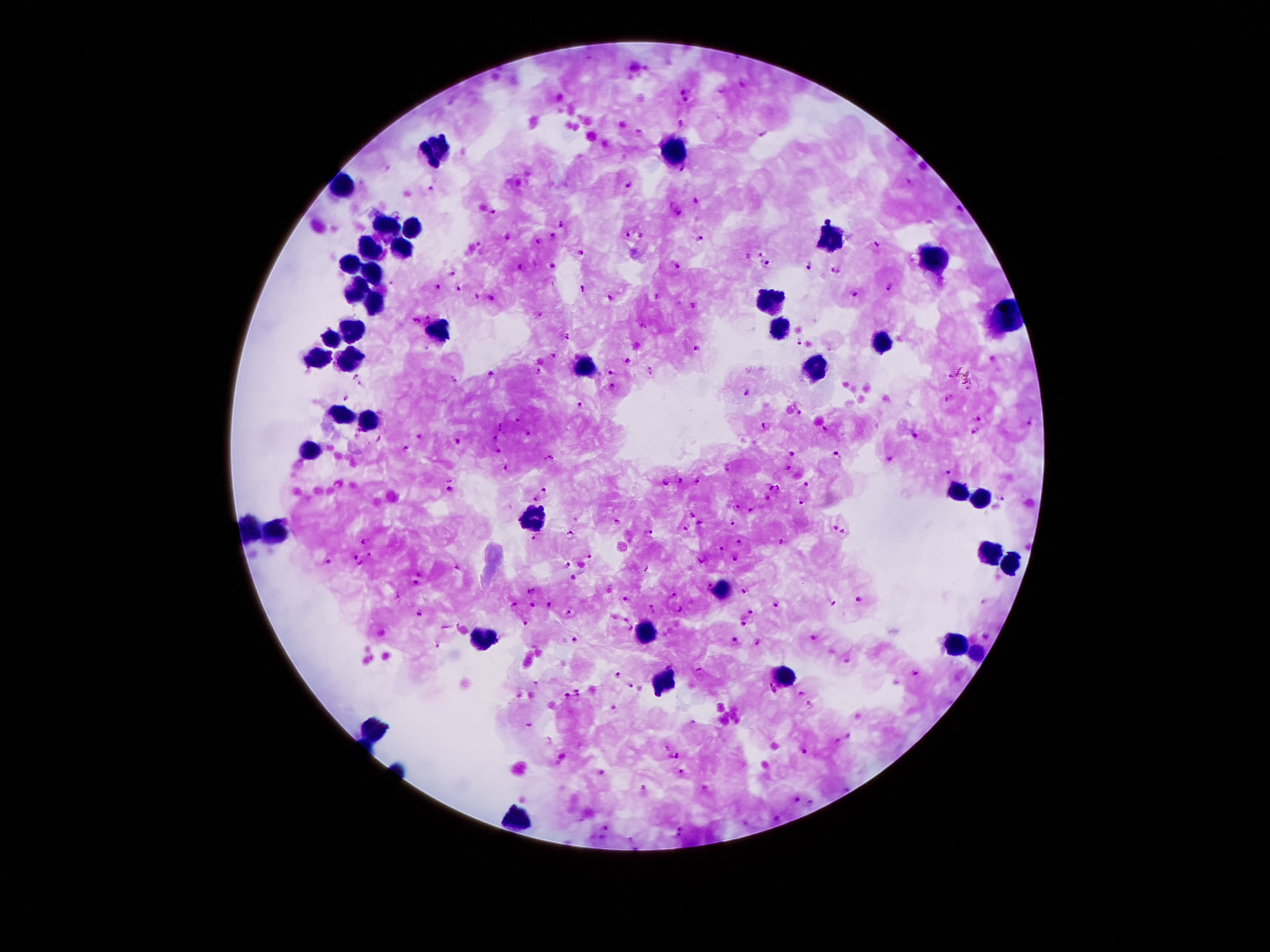
field_of_view: one from this slide
patient_malaria_status: infected with Plasmodium falciparum
malaria_parasite_locations: 'approximate object centers, in pixels from the top-left corner: (x=742, y=85), (x=681, y=93), (x=686, y=100), (x=683, y=124), (x=685, y=170), (x=630, y=184), (x=431, y=190), (x=698, y=202), (x=672, y=205), (x=959, y=211), (x=495, y=212), (x=681, y=214), (x=561, y=225), (x=628, y=235), (x=642, y=235), (x=552, y=236), (x=507, y=237), (x=701, y=239), (x=539, y=242), (x=877, y=244), (x=581, y=252), (x=761, y=255), (x=748, y=258), (x=553, y=265), (x=675, y=265), (x=768, y=265), (x=523, y=267), (x=809, y=267), (x=453, y=273), (x=834, y=273), (x=392, y=284), (x=439, y=288), (x=459, y=288), (x=890, y=288), (x=581, y=290), (x=856, y=294), (x=477, y=296), (x=492, y=297), (x=658, y=297), (x=612, y=299), (x=694, y=306), (x=537, y=315), (x=429, y=320), (x=414, y=322), (x=643, y=325), (x=567, y=335), (x=798, y=342), (x=696, y=350), (x=553, y=354), (x=628, y=361), (x=611, y=372), (x=650, y=372), (x=491, y=373), (x=538, y=373), (x=949, y=376), (x=357, y=378), (x=455, y=380), (x=362, y=386), (x=612, y=388), (x=748, y=394), (x=346, y=398), (x=949, y=400), (x=579, y=405), (x=800, y=414), (x=977, y=419), (x=517, y=421), (x=1030, y=423), (x=765, y=426), (x=501, y=427), (x=825, y=430), (x=975, y=432), (x=359, y=433), (x=528, y=435), (x=420, y=436), (x=914, y=436), (x=496, y=439), (x=458, y=441), (x=406, y=449), (x=499, y=451), (x=793, y=454), (x=836, y=454), (x=890, y=459), (x=552, y=461), (x=506, y=467), (x=788, y=468), (x=728, y=469), (x=946, y=470), (x=681, y=481), (x=698, y=481), (x=664, y=482), (x=808, y=484), (x=768, y=485), (x=453, y=486), (x=780, y=488), (x=545, y=491), (x=767, y=498), (x=537, y=499), (x=1002, y=499), (x=801, y=503), (x=737, y=506), (x=752, y=508), (x=691, y=515), (x=732, y=522), (x=618, y=523), (x=700, y=524), (x=836, y=527), (x=685, y=528), (x=845, y=532), (x=650, y=533), (x=569, y=536), (x=368, y=539), (x=534, y=539), (x=741, y=541), (x=780, y=542), (x=722, y=548), (x=371, y=556), (x=589, y=556), (x=356, y=557), (x=736, y=558), (x=702, y=560), (x=328, y=561), (x=361, y=564), (x=569, y=565), (x=419, y=574), (x=573, y=577), (x=416, y=585), (x=708, y=587), (x=745, y=591), (x=530, y=592), (x=676, y=594), (x=861, y=599), (x=626, y=600), (x=831, y=604), (x=512, y=605), (x=549, y=605), (x=778, y=605), (x=533, y=606), (x=654, y=609), (x=681, y=609), (x=753, y=611), (x=569, y=612), (x=420, y=613), (x=614, y=617), (x=626, y=619), (x=746, y=623), (x=525, y=624), (x=630, y=628), (x=984, y=636), (x=811, y=638), (x=574, y=640), (x=737, y=641), (x=759, y=642), (x=438, y=643), (x=848, y=660), (x=698, y=670), (x=915, y=672), (x=618, y=674), (x=631, y=685), (x=773, y=688), (x=579, y=693), (x=801, y=694), (x=567, y=696), (x=809, y=705), (x=692, y=723), (x=529, y=726), (x=848, y=736), (x=838, y=740), (x=667, y=749), (x=804, y=753), (x=675, y=757), (x=601, y=773), (x=681, y=774), (x=643, y=789), (x=795, y=801), (x=812, y=803), (x=777, y=818), (x=681, y=832), (x=631, y=839)'
leukocyte_locations: 'approximate object centers, in pixels from the top-left corner: (x=437, y=151), (x=674, y=151), (x=342, y=184), (x=385, y=228), (x=412, y=228), (x=829, y=236), (x=370, y=251), (x=402, y=251), (x=933, y=263), (x=347, y=264), (x=370, y=275), (x=357, y=291), (x=373, y=303), (x=768, y=305), (x=1010, y=316), (x=776, y=327), (x=348, y=330), (x=435, y=332), (x=331, y=338), (x=880, y=344), (x=319, y=358), (x=345, y=360), (x=582, y=366), (x=811, y=369), (x=342, y=415), (x=367, y=419), (x=313, y=451), (x=959, y=495), (x=982, y=500), (x=535, y=520), (x=249, y=528), (x=276, y=531), (x=990, y=555), (x=1013, y=563), (x=724, y=591), (x=646, y=634), (x=483, y=642), (x=958, y=647), (x=974, y=656), (x=784, y=675), (x=664, y=683), (x=371, y=728), (x=516, y=823)'
capture: smartphone camera through the microscope eyepiece
image_size: 1270×952 pixels
magnification: 100x
stain: Giemsa
preparation: thick blood film